Assess this cell for malaria.
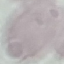
Uninfected.

preparation = thin blood film
stain = Giemsa
image type = cell patch, automatically extracted from a larger field of view and resized to 64 × 64 pixels
capture = smartphone through the microscope eyepiece